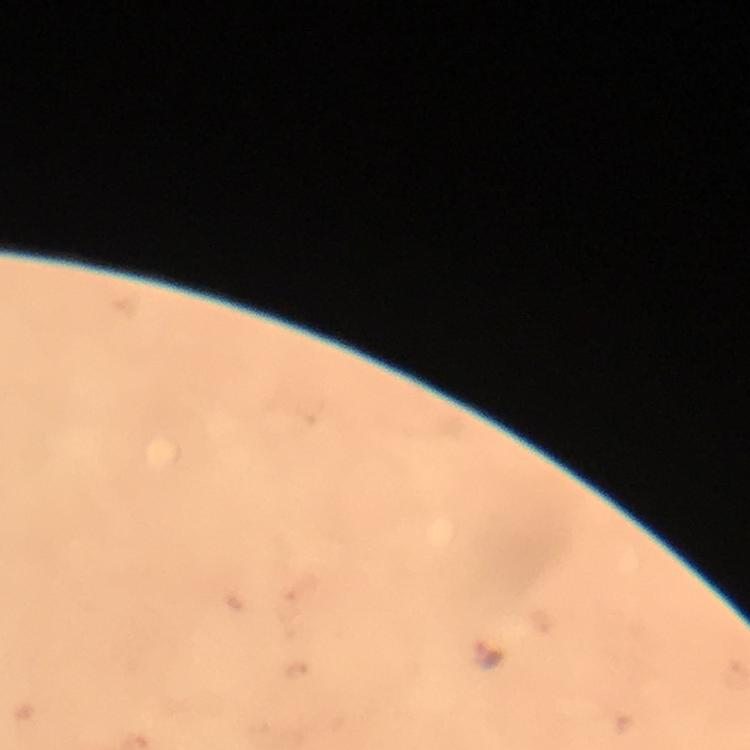
{
  "stain": "Giemsa",
  "plasmodium_parasite_locations": "approximate centers as [x, y] in pixels: [488, 653]",
  "cropped_from": "a single field of view",
  "context": "from a malaria diagnostic workup",
  "image_size": "750×750 pixels",
  "magnification": "100x",
  "preparation": "thick smear",
  "immersion_oil": "applied",
  "capture": "smartphone mounted on the microscope"
}